Give the position of every leukocyte visible.
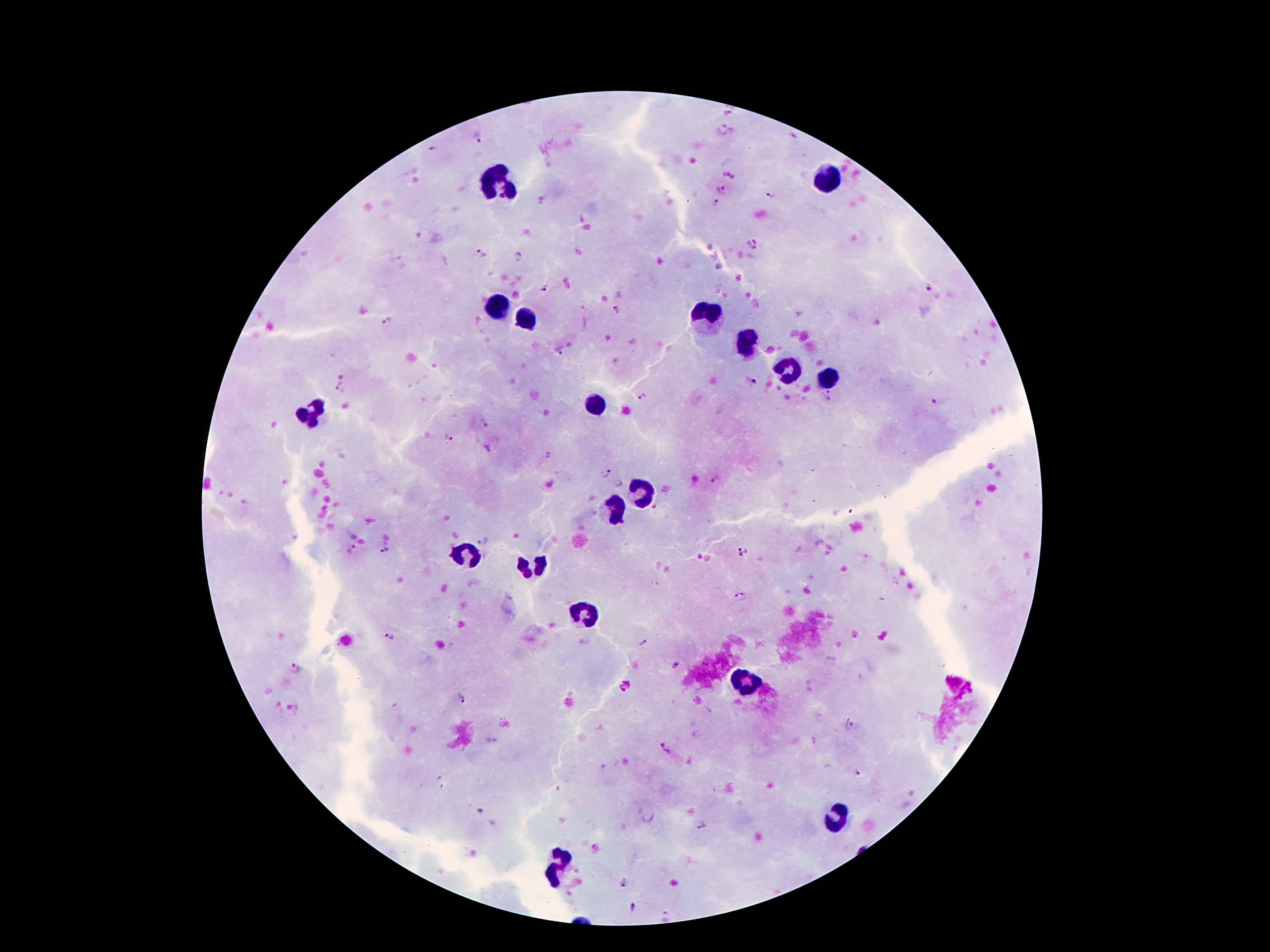

Approximate centers as {x, y} in pixels.
Leukocytes: {494, 177}, {828, 182}, {497, 308}, {709, 315}, {526, 318}, {749, 345}, {788, 372}, {830, 380}, {596, 402}, {309, 409}, {643, 488}, {610, 506}, {472, 555}, {531, 565}, {586, 614}, {746, 681}, {839, 817}, {560, 869}.

Plasmodium parasite locations: {721, 129}, {479, 139}, {433, 149}, {722, 192}, {771, 196}, {715, 204}, {752, 243}, {478, 253}, {520, 255}, {718, 266}, {545, 288}, {929, 290}, {617, 310}, {386, 321}, {560, 350}, {754, 382}, {341, 388}, {830, 395}, {641, 399}, {935, 401}, {484, 423}, {449, 438}, {605, 472}, {715, 479}, {619, 485}, {483, 541}, {352, 549}, {385, 550}, {736, 551}, {740, 595}, {389, 637}, {643, 642}, {678, 663}, {297, 666}, {461, 699}, {848, 727}, {492, 741}, {663, 750}, {858, 771}, {482, 810}, {701, 823}, {624, 882}, {633, 907}, {665, 916}. Patient malaria status: positive for Plasmodium falciparum. Image is 1270×952 pixels. Single field of view. 100x magnification. Smartphone photograph taken through the microscope eyepiece. Thick blood smear. Giemsa stain.